Describe the morphology of the erythrocytes.
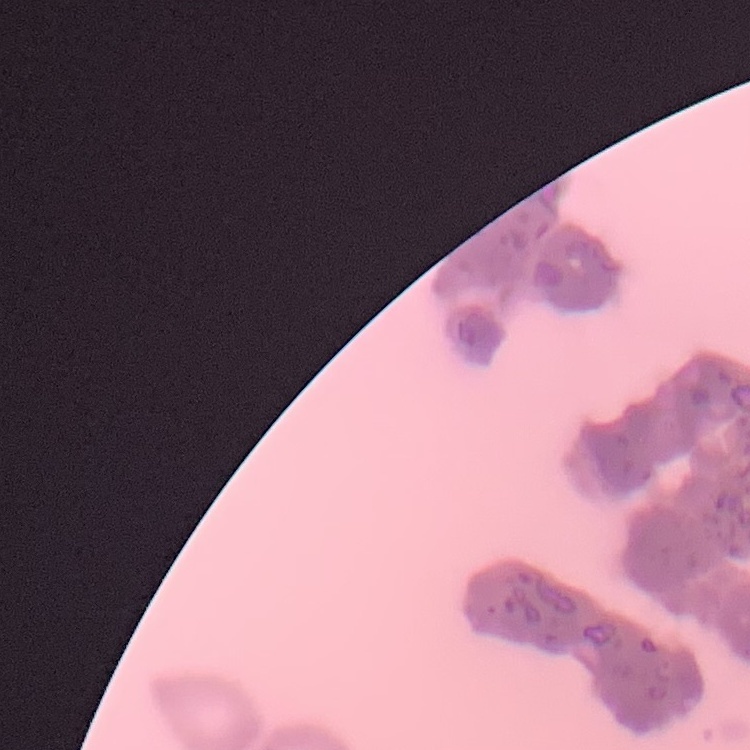
They show rouleaux formation.

Summary:
  - Preparation: thin blood film
  - Image type: one tile cut from a larger photomicrograph
  - Stain: Field's or Giemsa